Locate every Plasmodium ovale-infected red blood cell.
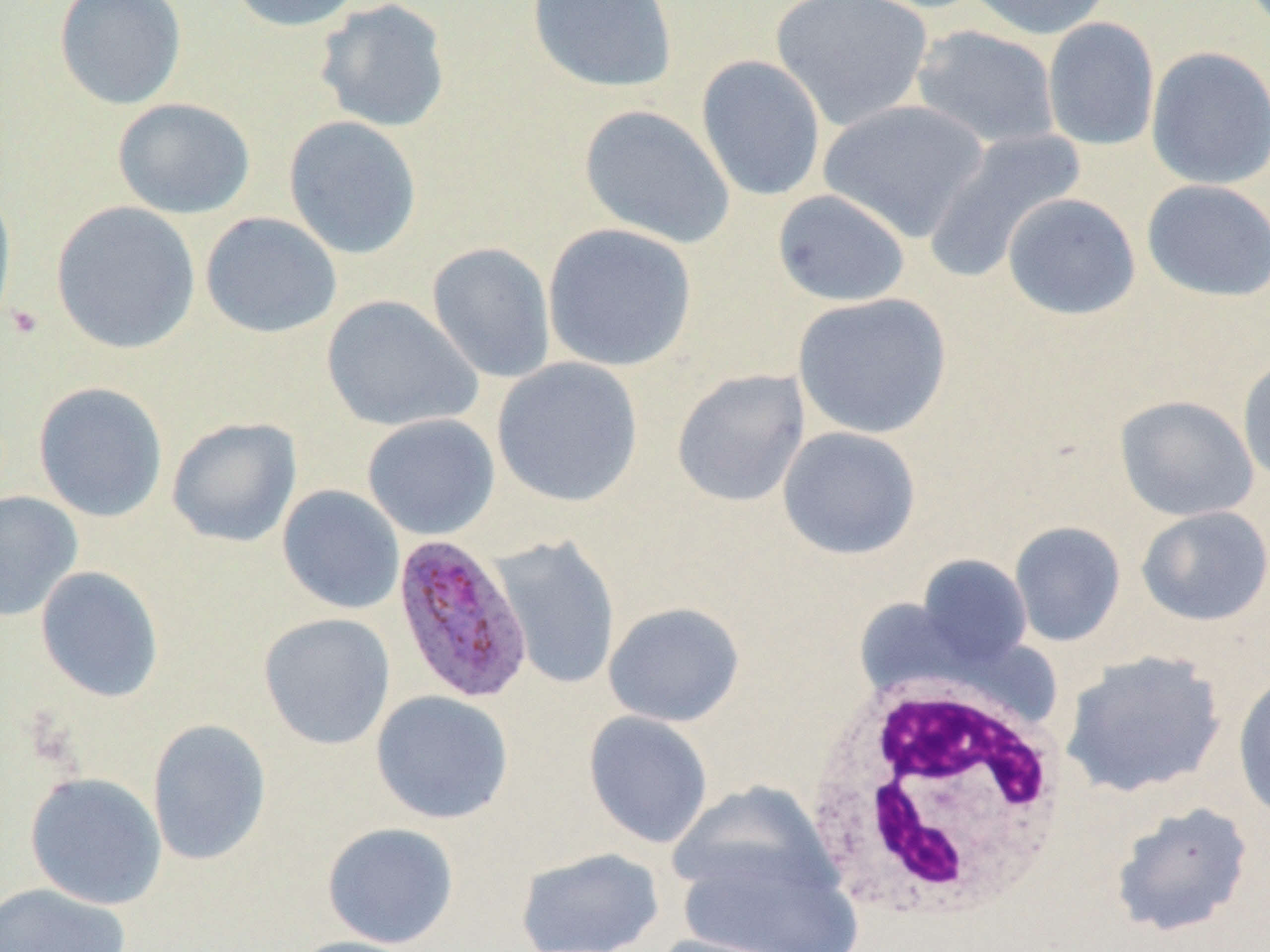
Approximate bounding boxes as (x1, y1, x2, y2) in pixels.
Plasmodium ovale-infected red blood cells: (391, 533, 534, 704).

Summary:
  - Uninfected red blood cell locations: (54, 0, 187, 110), (224, 0, 367, 33), (527, 0, 678, 93), (769, 0, 933, 131), (965, 0, 1115, 40), (314, 1, 453, 133), (1042, 17, 1160, 151), (910, 24, 1060, 151), (1145, 46, 1270, 190), (696, 54, 826, 202), (112, 98, 255, 219), (819, 99, 990, 243), (578, 104, 735, 249), (283, 115, 423, 259), (923, 127, 1087, 284), (1141, 179, 1270, 302), (0, 185, 18, 332), (772, 188, 910, 307), (1002, 193, 1141, 320), (51, 201, 201, 354), (199, 211, 342, 338), (542, 222, 697, 372), (426, 242, 556, 383), (793, 292, 952, 439), (320, 295, 483, 433), (1237, 354, 1270, 487), (491, 358, 644, 507), (671, 368, 810, 508), (32, 381, 168, 522), (1114, 395, 1259, 522), (361, 413, 500, 541), (166, 416, 302, 547), (777, 426, 921, 560), (277, 485, 406, 615), (0, 491, 83, 623), (1136, 506, 1270, 627), (1009, 521, 1126, 647), (490, 535, 621, 691), (916, 555, 1033, 668), (35, 566, 165, 703), (603, 601, 745, 727), (258, 612, 396, 750), (1060, 650, 1227, 799), (1232, 672, 1270, 821), (370, 690, 514, 825), (583, 711, 714, 849), (147, 718, 272, 866), (24, 771, 167, 910), (668, 781, 838, 903), (1109, 800, 1255, 939), (321, 821, 459, 949), (515, 847, 665, 952), (678, 848, 860, 951), (0, 882, 131, 952), (650, 933, 797, 952), (284, 935, 427, 952)
  - White blood cell locations: (801, 677, 1075, 928)
  - Platelet locations: (5, 304, 44, 339)
  - Slide-level diagnosis: Plasmodium ovale
  - Image size: 1270×952 pixels
  - Modality: optical microscopy
  - Preparation: thin blood smear
  - Magnification: 1000x
  - Field of view: single